Locate every blood parasite and identify its species.
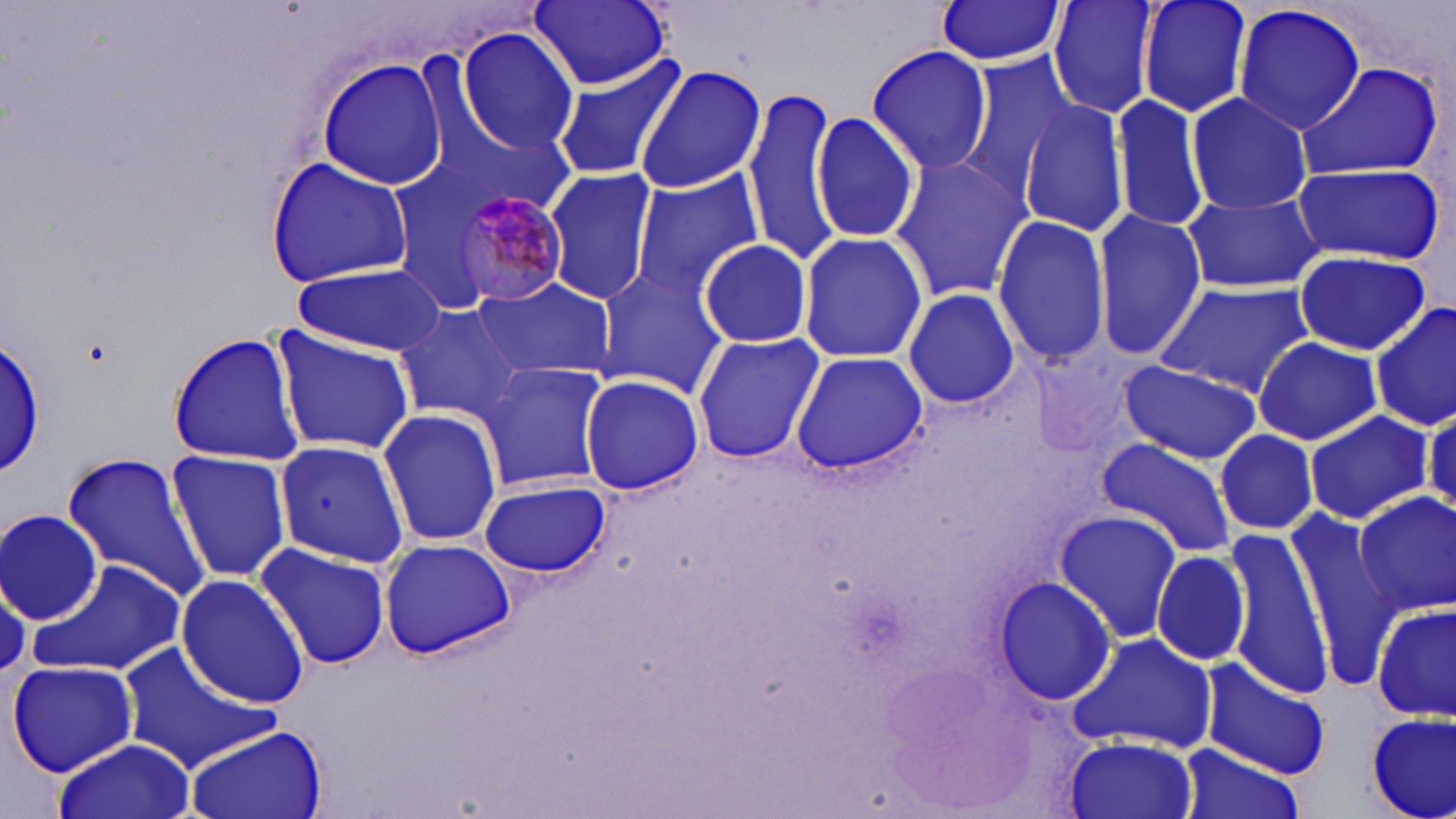
Approximate bounding boxes as named x1/y1/x2/y2 corners in pixels.
Plasmodium malariae-infected red blood cells: (x1=448, y1=187, x2=579, y2=311).
No Plasmodium falciparum, Plasmodium ovale, Plasmodium vivax, Babesia divergens, or Trypanosoma brucei observed.

{
  "slide_level_diagnosis": "Plasmodium malariae",
  "image_size": "1456×819 pixels",
  "modality": "optical microscopy",
  "uninfected_red_blood_cell_locations": "approximate bounding boxes as named x1/y1/x2/y2 corners in pixels: (x1=528, y1=0, x2=672, y2=89), (x1=1047, y1=0, x2=1162, y2=120), (x1=1137, y1=0, x2=1253, y2=120), (x1=932, y1=1, x2=1067, y2=65), (x1=1232, y1=3, x2=1367, y2=136), (x1=454, y1=28, x2=581, y2=155), (x1=864, y1=45, x2=994, y2=174), (x1=551, y1=53, x2=685, y2=185), (x1=953, y1=53, x2=1077, y2=203), (x1=314, y1=59, x2=451, y2=189), (x1=1296, y1=61, x2=1444, y2=180), (x1=635, y1=63, x2=768, y2=195), (x1=1110, y1=92, x2=1210, y2=234), (x1=743, y1=93, x2=841, y2=262), (x1=1184, y1=94, x2=1315, y2=215), (x1=1019, y1=99, x2=1129, y2=240), (x1=811, y1=110, x2=920, y2=244), (x1=890, y1=152, x2=1030, y2=303), (x1=266, y1=156, x2=413, y2=285), (x1=1290, y1=158, x2=1446, y2=267), (x1=543, y1=168, x2=658, y2=306), (x1=629, y1=169, x2=765, y2=294), (x1=1179, y1=190, x2=1325, y2=295), (x1=1093, y1=209, x2=1206, y2=359), (x1=991, y1=213, x2=1112, y2=366), (x1=798, y1=232, x2=927, y2=362), (x1=696, y1=238, x2=812, y2=349), (x1=1290, y1=250, x2=1432, y2=354), (x1=292, y1=264, x2=446, y2=355), (x1=593, y1=265, x2=730, y2=397), (x1=473, y1=277, x2=616, y2=382), (x1=1154, y1=280, x2=1317, y2=399), (x1=903, y1=288, x2=1024, y2=412), (x1=1370, y1=299, x2=1456, y2=431), (x1=390, y1=304, x2=527, y2=423), (x1=269, y1=327, x2=416, y2=455), (x1=165, y1=329, x2=305, y2=466), (x1=691, y1=332, x2=823, y2=465), (x1=0, y1=333, x2=49, y2=482), (x1=1252, y1=336, x2=1383, y2=446), (x1=792, y1=352, x2=927, y2=472), (x1=1115, y1=360, x2=1261, y2=463), (x1=476, y1=361, x2=611, y2=493), (x1=578, y1=372, x2=703, y2=496), (x1=377, y1=408, x2=503, y2=547), (x1=1303, y1=409, x2=1434, y2=525), (x1=1213, y1=428, x2=1319, y2=536), (x1=272, y1=438, x2=411, y2=570), (x1=1097, y1=439, x2=1238, y2=557), (x1=164, y1=449, x2=294, y2=581), (x1=61, y1=451, x2=212, y2=600), (x1=478, y1=479, x2=612, y2=579), (x1=1351, y1=493, x2=1456, y2=617), (x1=1, y1=507, x2=105, y2=624), (x1=1056, y1=509, x2=1180, y2=643), (x1=1286, y1=520, x2=1400, y2=685), (x1=1227, y1=529, x2=1332, y2=694), (x1=378, y1=536, x2=518, y2=660), (x1=253, y1=540, x2=392, y2=671), (x1=1151, y1=548, x2=1251, y2=669), (x1=31, y1=557, x2=191, y2=681), (x1=175, y1=573, x2=308, y2=708), (x1=991, y1=574, x2=1119, y2=706), (x1=0, y1=582, x2=28, y2=677), (x1=1370, y1=601, x2=1455, y2=722), (x1=1070, y1=633, x2=1216, y2=753), (x1=116, y1=642, x2=280, y2=776), (x1=7, y1=659, x2=140, y2=776), (x1=1200, y1=660, x2=1331, y2=777), (x1=1365, y1=711, x2=1455, y2=819), (x1=183, y1=725, x2=326, y2=819), (x1=1065, y1=735, x2=1199, y2=819), (x1=52, y1=736, x2=197, y2=819), (x1=1180, y1=745, x2=1303, y2=819)",
  "preparation": "thin blood smear",
  "stain": "May-Grünwald-Giemsa",
  "magnification": "1000x",
  "field_of_view": "single"
}